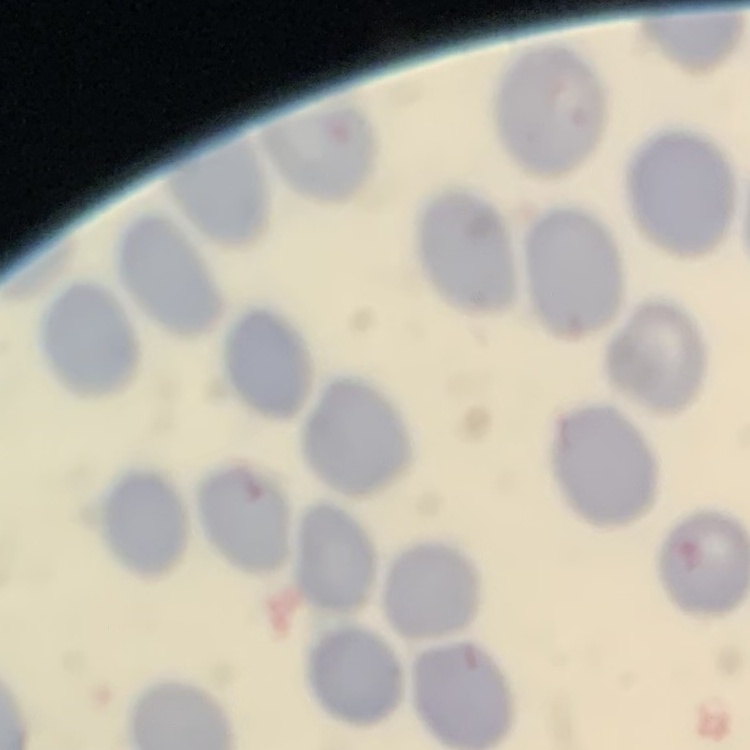
Summary:
  - Erythrocyte morphology: no rouleaux formation
  - Stain: Field's or Giemsa
  - Preparation: thin blood film
  - Image type: one tile cut from a larger photomicrograph